Identify the cell.
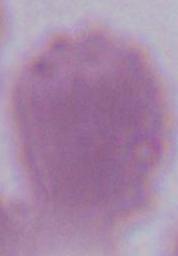

This is an erythrocyte.

Micrograph. Captured at 1000x magnification.